Locate every Plasmodium parasite.
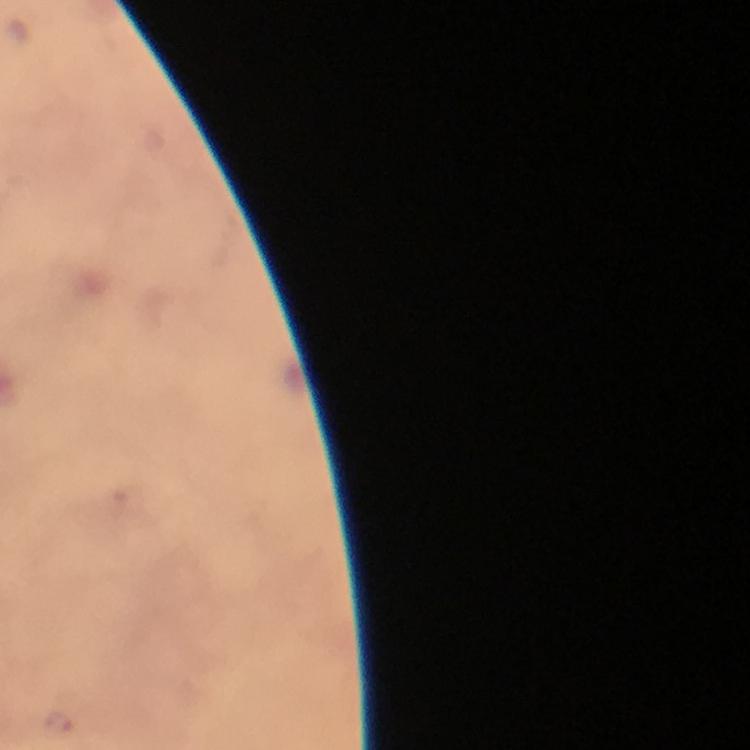

Approximate centers as [x, y] in pixels.
Plasmodium parasites: [58, 724].

Cropped region of a single field of view. From a malaria diagnostic workup. Immersion oil applied. Giemsa stain. Thick blood smear. At 100x magnification. Smartphone photograph taken through a microscope. Image is 750×750 pixels.